Assess this cell for malaria.
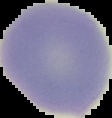
It is uninfected.

preparation = thin blood smear
image size = 112×118 pixels
image type = segmented cell region on a black background